Give the extent of all Plasmodium ovale-infected red blood cells.
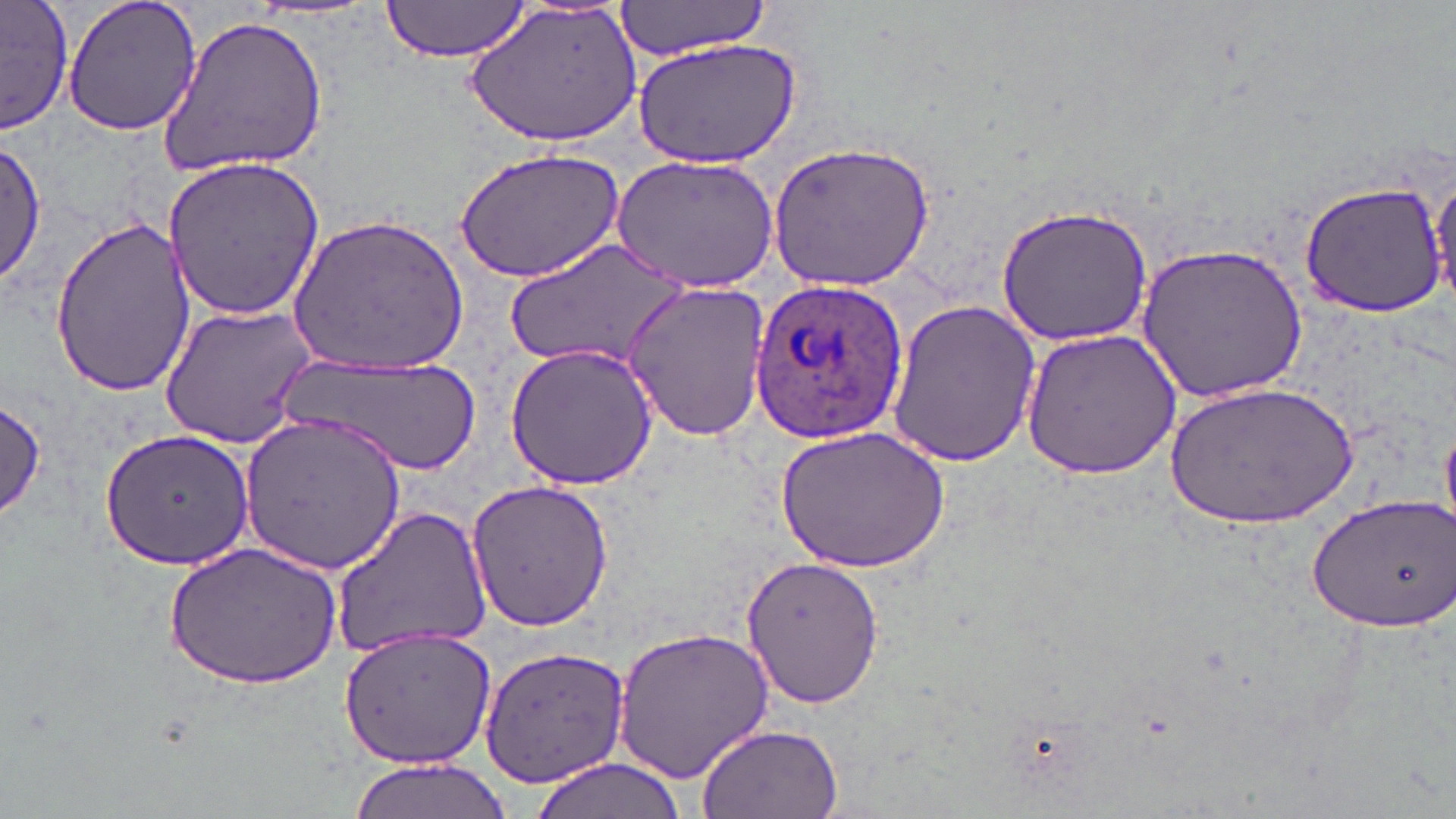
Approximate bounding boxes as named x1/y1/x2/y2 corners in pixels.
Plasmodium ovale-infected red blood cells: (x1=749, y1=275, x2=910, y2=446).

{
  "slide_level_diagnosis": "Plasmodium ovale",
  "image_size": "1456×819 pixels",
  "stain": "May-Grünwald-Giemsa",
  "uninfected_red_blood_cell_locations": "approximate bounding boxes as named x1/y1/x2/y2 corners in pixels: (x1=0, y1=0, x2=72, y2=137), (x1=61, y1=0, x2=204, y2=137), (x1=379, y1=0, x2=537, y2=63), (x1=469, y1=0, x2=642, y2=150), (x1=612, y1=1, x2=777, y2=59), (x1=160, y1=12, x2=329, y2=177), (x1=630, y1=37, x2=804, y2=171), (x1=1, y1=141, x2=47, y2=287), (x1=768, y1=141, x2=935, y2=291), (x1=455, y1=148, x2=625, y2=284), (x1=613, y1=154, x2=780, y2=291), (x1=162, y1=155, x2=326, y2=321), (x1=1428, y1=168, x2=1456, y2=306), (x1=1300, y1=179, x2=1450, y2=318), (x1=995, y1=204, x2=1153, y2=346), (x1=291, y1=211, x2=472, y2=375), (x1=49, y1=219, x2=192, y2=393), (x1=503, y1=238, x2=692, y2=375), (x1=1135, y1=243, x2=1309, y2=405), (x1=622, y1=279, x2=772, y2=443), (x1=885, y1=299, x2=1043, y2=467), (x1=158, y1=304, x2=321, y2=445), (x1=1019, y1=325, x2=1184, y2=481), (x1=504, y1=342, x2=656, y2=491), (x1=275, y1=351, x2=485, y2=477), (x1=1174, y1=378, x2=1355, y2=529), (x1=0, y1=397, x2=47, y2=521), (x1=241, y1=413, x2=409, y2=574), (x1=1440, y1=417, x2=1455, y2=536), (x1=775, y1=426, x2=949, y2=574), (x1=100, y1=427, x2=258, y2=571), (x1=463, y1=480, x2=615, y2=630), (x1=1304, y1=491, x2=1455, y2=634), (x1=331, y1=508, x2=493, y2=655), (x1=162, y1=543, x2=341, y2=687), (x1=740, y1=554, x2=883, y2=712), (x1=333, y1=622, x2=496, y2=770), (x1=614, y1=622, x2=777, y2=786), (x1=475, y1=642, x2=632, y2=788), (x1=695, y1=723, x2=844, y2=818), (x1=525, y1=757, x2=691, y2=819), (x1=343, y1=760, x2=513, y2=819)",
  "field_of_view": "one of a larger specimen",
  "modality": "light microscopy",
  "preparation": "thin blood film",
  "magnification": "1000x"
}